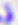 Photomicrograph. Captured at 400x magnification. Toxoplasma gondii is shown.